Report the malaria status of this cell.
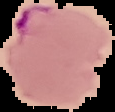

It is parasitized.

{
  "image_type": "segmented cell region with the area outside set to black",
  "preparation": "thin blood film",
  "image_size": "115×112 pixels"
}